Identify the preparation type.
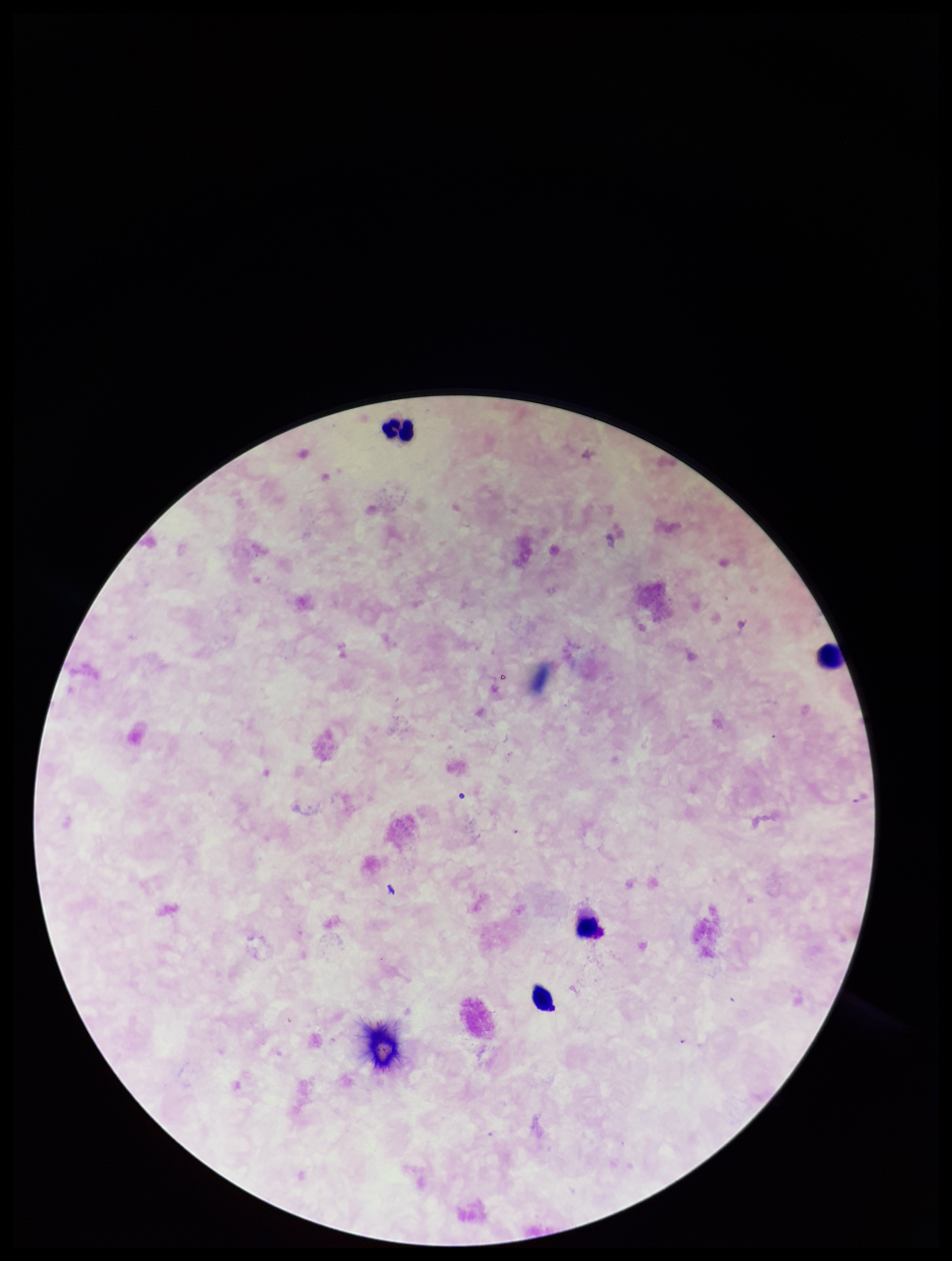

It is a thick blood smear.

Image is 952×1261 pixels. Single field of view. Plasmodium parasites: none seen. Leukocyte count: 4. Photographed through the microscope eyepiece with a smartphone camera. Patient malaria status: negative. Stained with Giemsa. Parasite count: 0.